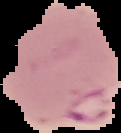
Result: Plasmodium parasites identified. Cell region segmented out of the field of view; the surrounding area is masked to black. Image is 121×133 pixels. From a thin blood film.